Describe the morphology of the erythrocytes.
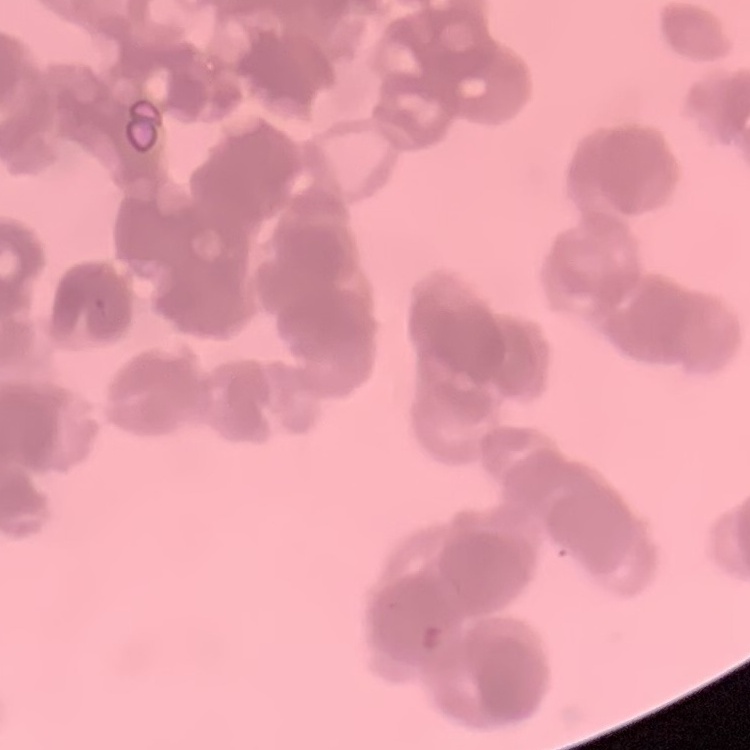

They show rouleaux formation.

preparation = thin peripheral smear
image type = one tile cut from a larger photomicrograph
stain = Field's or Giemsa